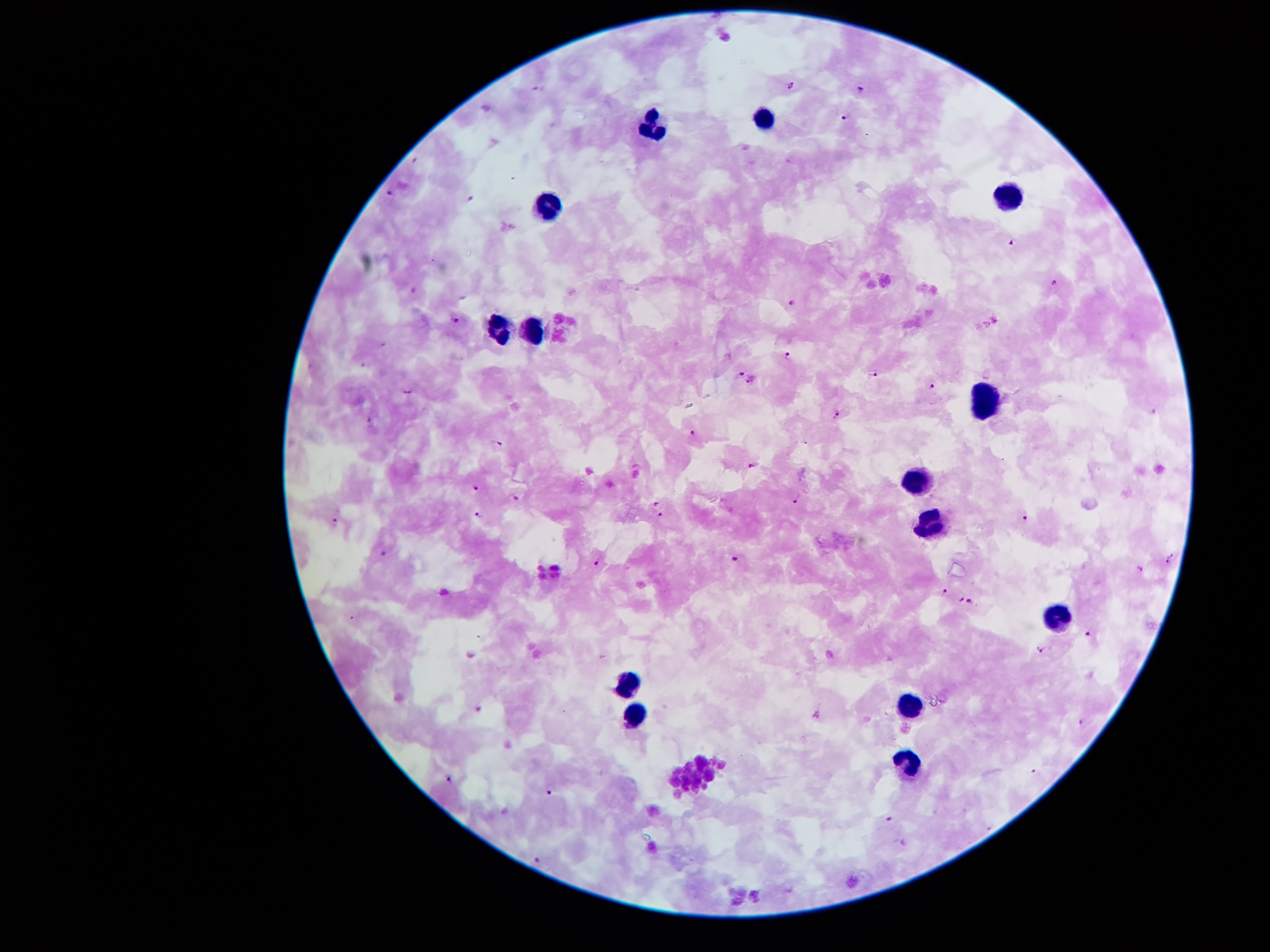 Approximate centers as [x, y] in pixels. Leukocyte locations: [764, 117], [654, 122], [1003, 195], [548, 207], [495, 328], [537, 331], [990, 403], [917, 477], [929, 522], [1056, 620], [629, 686], [915, 704], [633, 721], [909, 768]. Plasmodium parasite locations: [793, 85], [860, 89], [844, 118], [390, 191], [470, 197], [1013, 242], [1055, 282], [791, 303], [456, 319], [789, 354], [742, 371], [875, 375], [751, 380], [932, 384], [408, 390], [838, 414], [692, 432], [497, 444], [751, 464], [476, 488], [515, 498], [797, 499], [656, 502], [659, 514], [481, 515], [335, 518], [1026, 518], [385, 552], [1172, 553], [736, 557], [598, 561], [1168, 561], [1140, 568], [945, 592], [962, 600], [970, 600], [1089, 634], [1042, 648], [1082, 721], [1035, 771], [451, 778], [549, 792], [891, 818], [538, 859]. Smartphone photograph taken through the microscope eyepiece. Image is 1270×952 pixels. Giemsa-stained preparation. Patient malaria status: infected with Plasmodium falciparum. One field from this slide. 100x magnification. Thick blood film.